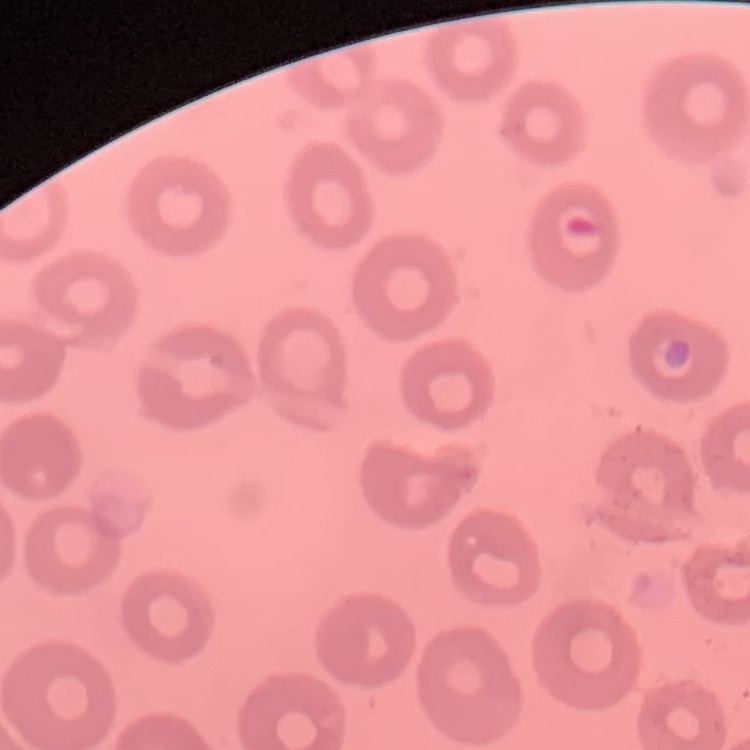
Summary:
  - Red blood cell morphology: no rouleaux formation
  - Preparation: thin blood film
  - Stain: Field's or Giemsa
  - Image type: square crop of a larger photomicrograph